Outline every leukocyte.
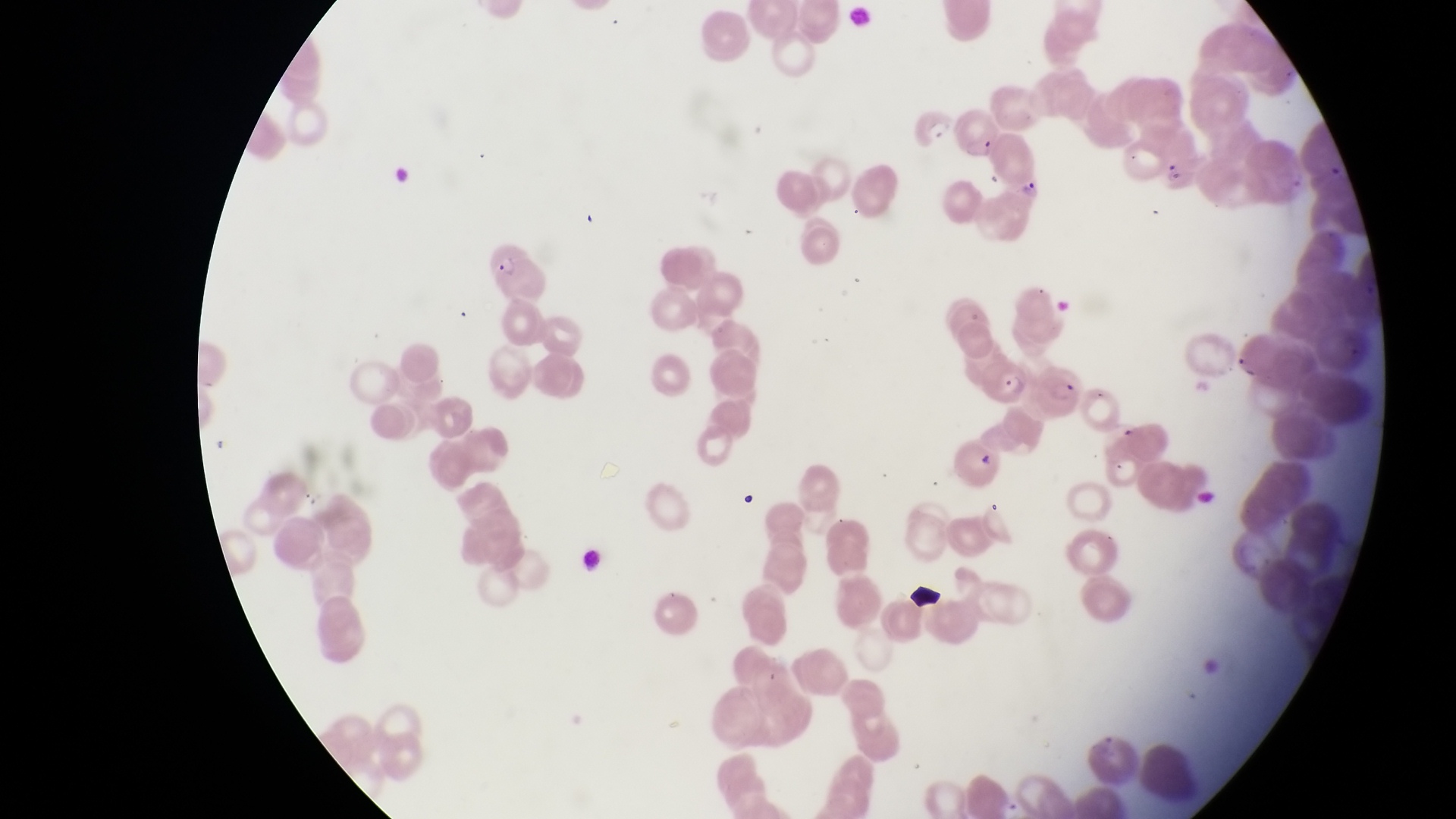

No leukocytes observed.

parasitised red blood cell locations = approximate bounding boxes as left top right bottom in pixels: 485 245 559 304; 981 354 1033 406; 1039 362 1085 421
preparation = thin blood smear
artifact (platelet-like body, stain precipitate, or debris) locations = approximate bounding boxes as left top right bottom in pixels: 980 452 1000 471; 909 582 949 614
capture = smartphone photograph through the eyepiece of an Olympus CX-23 microscope
trophozoite locations = approximate bounding boxes as left top right bottom in pixels: 917 113 956 145; 1160 162 1186 189; 1018 169 1047 203
magnification = 1000x
field of view = single
image size = 1456×819 pixels
country = Uganda